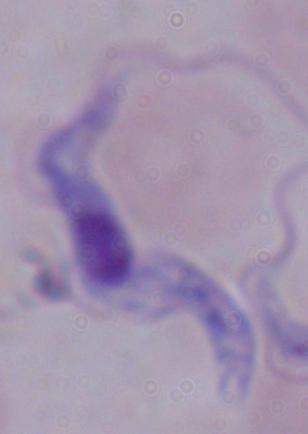

Captured at 1000x magnification. Micrograph. A trypanosome is seen.